Describe the morphology of the red blood cells.
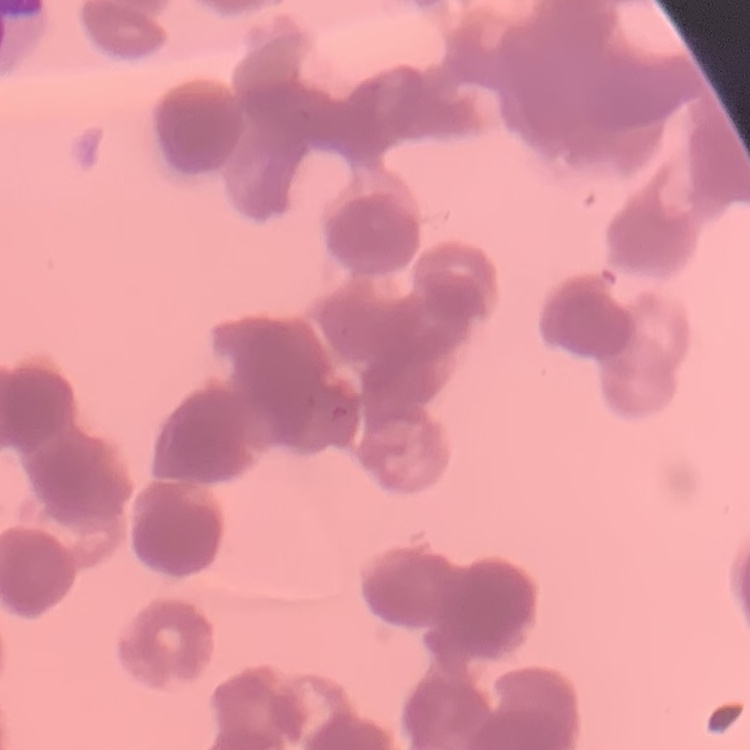
They show rouleaux formation.

Summary:
  - Preparation: thin blood smear
  - Stain: Field's or Giemsa
  - Image type: one tile cut from a larger photomicrograph